Outline each blood parasite and name the species.
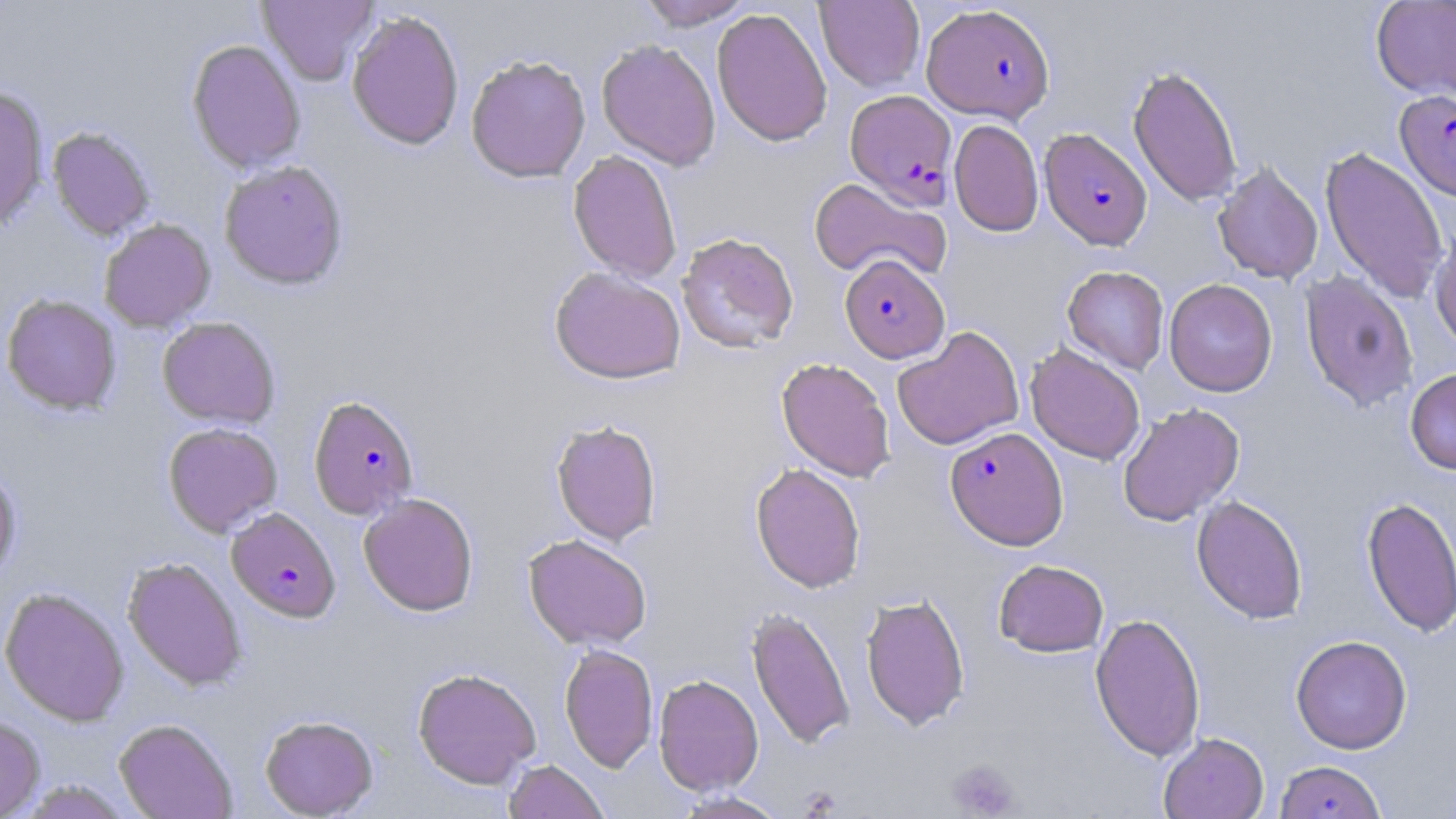
Approximate bounding boxes as (x1,y1)-(x2,y2) corner pairs in pixels.
Plasmodium falciparum-infected red blood cells: (922,3)-(1055,123), (1396,89)-(1456,201), (845,90)-(957,208), (1039,127)-(1152,250), (840,254)-(949,363), (308,396)-(419,520), (944,426)-(1068,550), (226,507)-(340,622), (1274,760)-(1387,819).
No Plasmodium ovale, Plasmodium malariae, Plasmodium vivax, Babesia divergens, or Trypanosoma brucei observed.

{
  "slide_level_diagnosis": "Plasmodium falciparum",
  "modality": "light microscopy",
  "preparation": "thin blood smear",
  "image_size": "1456×819 pixels",
  "magnification": "1000x",
  "platelet_locations": "approximate bounding boxes as (x1,y1)-(x2,y2) corner pairs in pixels: (946,759)-(1022,818)",
  "field_of_view": "single",
  "uninfected_red_blood_cell_locations": "approximate bounding boxes as (x1,y1)-(x2,y2) corner pairs in pixels: (257,0)-(378,84), (636,0)-(753,30), (814,0)-(925,92), (1371,0)-(1456,100), (712,7)-(832,146), (346,10)-(464,150), (187,39)-(306,173), (596,39)-(721,170), (465,53)-(591,183), (1128,64)-(1243,208), (0,86)-(49,234), (949,118)-(1044,237), (48,127)-(155,240), (1320,145)-(1449,304), (568,150)-(682,282), (219,160)-(349,290), (1212,161)-(1324,284), (808,177)-(950,283), (99,218)-(215,332), (1429,222)-(1456,353), (676,233)-(799,353), (1062,265)-(1169,374), (549,266)-(686,385), (1300,271)-(1419,412), (1164,278)-(1278,397), (2,295)-(122,415), (156,317)-(280,428), (891,326)-(1025,450), (1025,344)-(1145,465), (776,357)-(895,482), (1405,367)-(1456,474), (1118,403)-(1244,526), (550,419)-(662,545), (163,422)-(282,537), (751,463)-(866,593), (0,465)-(22,584), (358,493)-(479,616), (1191,495)-(1308,624), (1362,495)-(1456,638), (523,533)-(652,650), (123,556)-(246,691), (993,559)-(1109,657), (0,587)-(129,726), (860,593)-(970,730), (746,606)-(855,750), (1090,612)-(1206,761), (1290,635)-(1413,754), (559,643)-(658,773), (412,667)-(541,788), (653,673)-(764,795), (260,714)-(379,818), (0,716)-(45,818), (114,718)-(237,819), (1158,732)-(1269,819), (503,759)-(610,819), (14,779)-(132,818), (671,791)-(789,818)",
  "stain": "May-Grünwald-Giemsa"
}